Outline each blood parasite and name the species.
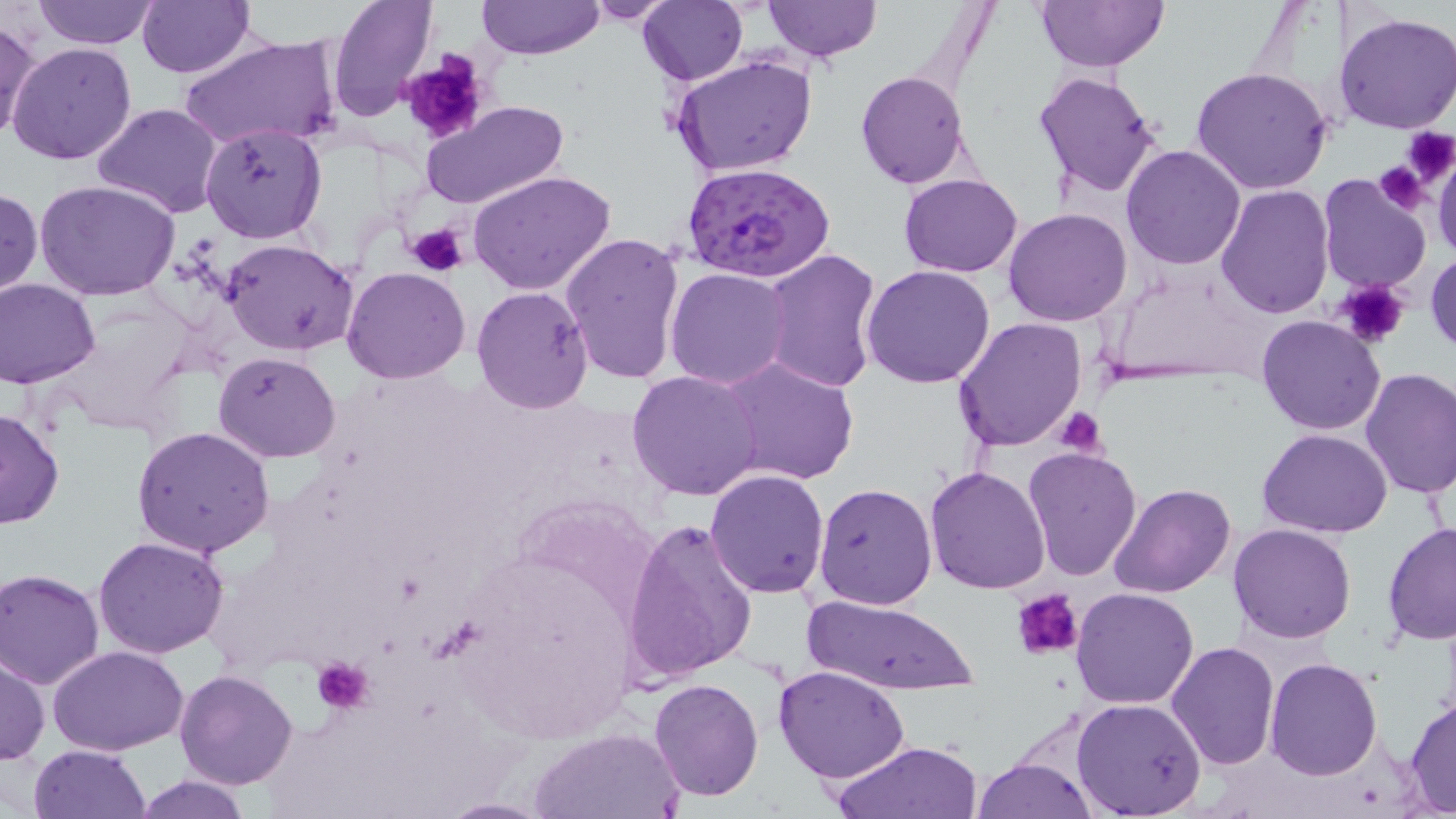

Approximate bounding boxes as named x1/y1/x2/y2 corners in pixels.
Plasmodium falciparum-infected red blood cells: (x1=679, y1=160, x2=834, y2=283).
No Plasmodium ovale, Plasmodium malariae, Plasmodium vivax, Babesia divergens, or Trypanosoma brucei observed.

Uninfected red blood cell locations: (x1=32, y1=0, x2=158, y2=49), (x1=136, y1=0, x2=253, y2=78), (x1=328, y1=0, x2=438, y2=122), (x1=476, y1=0, x2=603, y2=60), (x1=583, y1=0, x2=678, y2=24), (x1=765, y1=0, x2=880, y2=61), (x1=1034, y1=0, x2=1170, y2=73), (x1=638, y1=1, x2=747, y2=84), (x1=1334, y1=13, x2=1456, y2=135), (x1=1, y1=17, x2=41, y2=146), (x1=177, y1=33, x2=343, y2=152), (x1=7, y1=42, x2=137, y2=167), (x1=671, y1=53, x2=817, y2=178), (x1=1191, y1=67, x2=1335, y2=195), (x1=1031, y1=69, x2=1163, y2=199), (x1=854, y1=71, x2=971, y2=190), (x1=419, y1=101, x2=571, y2=212), (x1=91, y1=102, x2=224, y2=219), (x1=199, y1=123, x2=327, y2=243), (x1=1121, y1=144, x2=1246, y2=270), (x1=1432, y1=149, x2=1456, y2=266), (x1=470, y1=168, x2=617, y2=297), (x1=899, y1=173, x2=1022, y2=275), (x1=1317, y1=175, x2=1431, y2=294), (x1=36, y1=181, x2=183, y2=301), (x1=1216, y1=184, x2=1334, y2=321), (x1=0, y1=185, x2=43, y2=302), (x1=1004, y1=208, x2=1132, y2=327), (x1=561, y1=231, x2=688, y2=387), (x1=221, y1=238, x2=359, y2=355), (x1=759, y1=248, x2=882, y2=393), (x1=1426, y1=249, x2=1456, y2=357), (x1=862, y1=263, x2=996, y2=389), (x1=341, y1=265, x2=472, y2=385), (x1=665, y1=267, x2=792, y2=390), (x1=2, y1=278, x2=99, y2=388), (x1=471, y1=286, x2=596, y2=414), (x1=1257, y1=315, x2=1386, y2=437), (x1=954, y1=317, x2=1086, y2=451), (x1=214, y1=352, x2=341, y2=461), (x1=720, y1=357, x2=860, y2=486), (x1=1358, y1=368, x2=1456, y2=498), (x1=627, y1=369, x2=766, y2=502), (x1=1, y1=409, x2=65, y2=529), (x1=132, y1=424, x2=277, y2=559), (x1=1258, y1=428, x2=1393, y2=538), (x1=1023, y1=446, x2=1142, y2=581), (x1=924, y1=464, x2=1052, y2=594), (x1=705, y1=468, x2=829, y2=598), (x1=812, y1=482, x2=937, y2=611), (x1=1111, y1=483, x2=1237, y2=599), (x1=623, y1=516, x2=760, y2=685), (x1=1382, y1=521, x2=1456, y2=646), (x1=1229, y1=523, x2=1357, y2=643), (x1=93, y1=535, x2=229, y2=659), (x1=1, y1=569, x2=105, y2=689), (x1=1071, y1=588, x2=1199, y2=710), (x1=802, y1=594, x2=978, y2=693), (x1=1166, y1=641, x2=1281, y2=770), (x1=47, y1=644, x2=190, y2=754), (x1=0, y1=654, x2=48, y2=764), (x1=1264, y1=657, x2=1382, y2=779), (x1=772, y1=665, x2=911, y2=784), (x1=174, y1=670, x2=300, y2=789), (x1=648, y1=678, x2=765, y2=802), (x1=1403, y1=693, x2=1456, y2=816), (x1=1070, y1=698, x2=1207, y2=818), (x1=530, y1=726, x2=685, y2=817), (x1=829, y1=739, x2=983, y2=819), (x1=28, y1=744, x2=150, y2=819), (x1=971, y1=755, x2=1098, y2=818), (x1=133, y1=775, x2=253, y2=818), (x1=431, y1=796, x2=557, y2=818). Platelet locations: (x1=398, y1=53, x2=493, y2=146), (x1=1401, y1=128, x2=1456, y2=187), (x1=1373, y1=161, x2=1430, y2=214), (x1=407, y1=222, x2=468, y2=278), (x1=1332, y1=279, x2=1412, y2=349), (x1=1053, y1=405, x2=1107, y2=455), (x1=1012, y1=590, x2=1083, y2=662), (x1=311, y1=656, x2=374, y2=714). Slide-level diagnosis: Plasmodium falciparum. May-Grünwald-Giemsa stain. Thin blood smear. Image is 1456×819 pixels. Light microscopy. Captured at 1000x magnification. One field of a larger specimen.